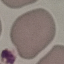

Summary:
  - Result: negative for malaria parasites
  - Stain: Giemsa
  - Capture: smartphone camera at the microscope eyepiece
  - Preparation: thin blood smear
  - Image type: automatically extracted cell patch, resized to 64 × 64 pixels